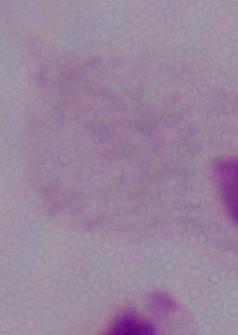
Summary:
  - Identification: trichomonad
  - Magnification: 1000x
  - Modality: micrograph